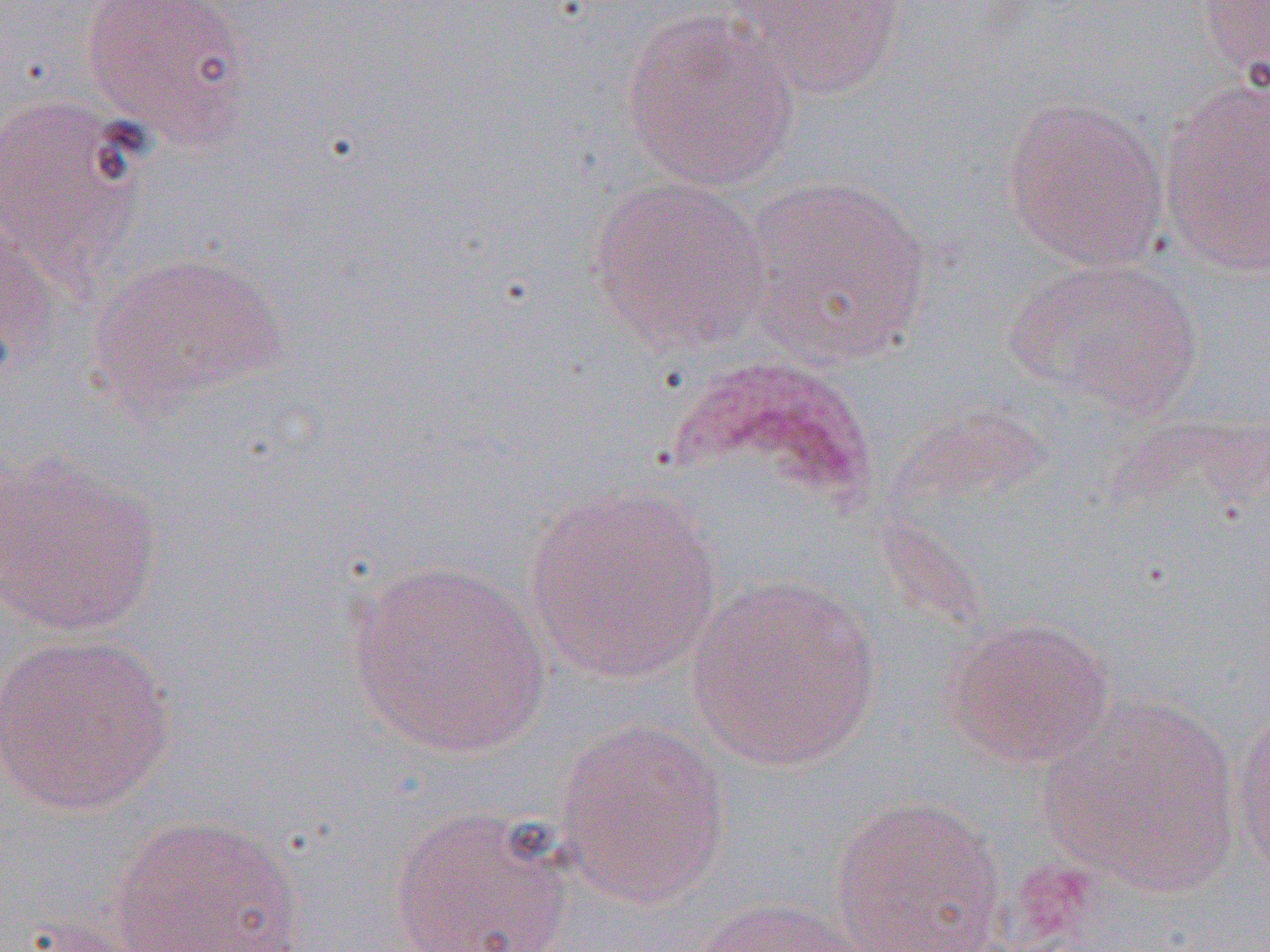

{
  "slide_level_diagnosis": "Plasmodium ovale",
  "uninfected_red_blood_cell_locations": "approximate bounding boxes as named x1/y1/x2/y2 corners in pixels: (x1=81, y1=0, x2=254, y2=149), (x1=729, y1=0, x2=908, y2=101), (x1=1196, y1=1, x2=1270, y2=81), (x1=620, y1=11, x2=800, y2=192), (x1=1159, y1=78, x2=1269, y2=277), (x1=0, y1=94, x2=147, y2=284), (x1=1001, y1=96, x2=1170, y2=271), (x1=587, y1=175, x2=773, y2=355), (x1=741, y1=175, x2=934, y2=367), (x1=1, y1=210, x2=63, y2=389), (x1=88, y1=251, x2=289, y2=416), (x1=1007, y1=257, x2=1203, y2=417), (x1=0, y1=448, x2=163, y2=636), (x1=522, y1=485, x2=723, y2=684), (x1=346, y1=560, x2=553, y2=759), (x1=686, y1=575, x2=883, y2=772), (x1=942, y1=616, x2=1115, y2=769), (x1=0, y1=630, x2=178, y2=815), (x1=1041, y1=695, x2=1243, y2=894), (x1=1232, y1=699, x2=1270, y2=882), (x1=553, y1=717, x2=731, y2=910), (x1=830, y1=794, x2=1007, y2=952), (x1=388, y1=805, x2=577, y2=952), (x1=106, y1=813, x2=309, y2=952), (x1=684, y1=896, x2=878, y2=952)",
  "image_size": "1270×952 pixels",
  "modality": "optical microscopy",
  "magnification": "1000x",
  "preparation": "thin blood film",
  "field_of_view": "one of a larger specimen"
}